Comment on the morphology of the erythrocytes.
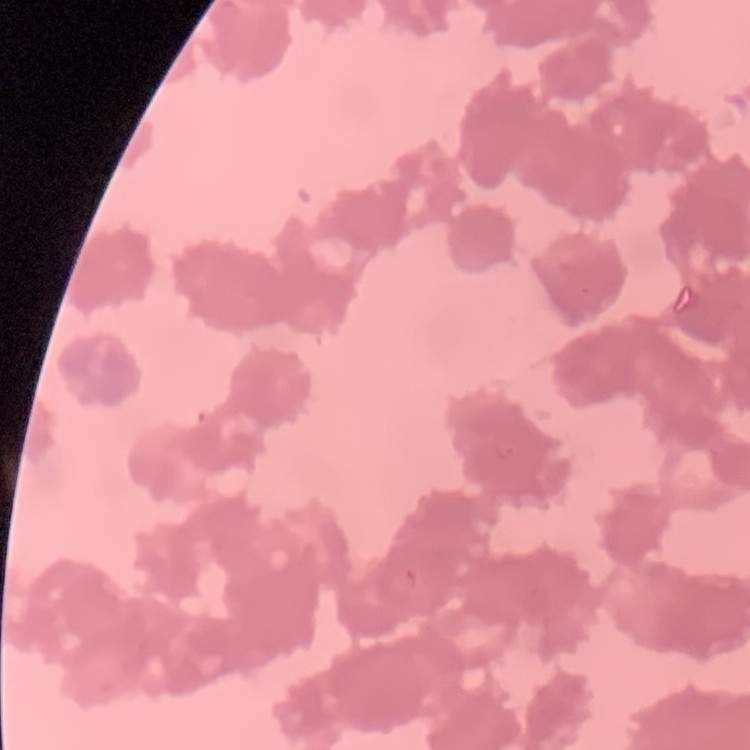

Rouleaux formation.

Summary:
  - Stain: Field's or Giemsa
  - Preparation: thin blood film
  - Image type: one tile cut from a larger photomicrograph